Locate every Plasmodium falciparum-infected red blood cell.
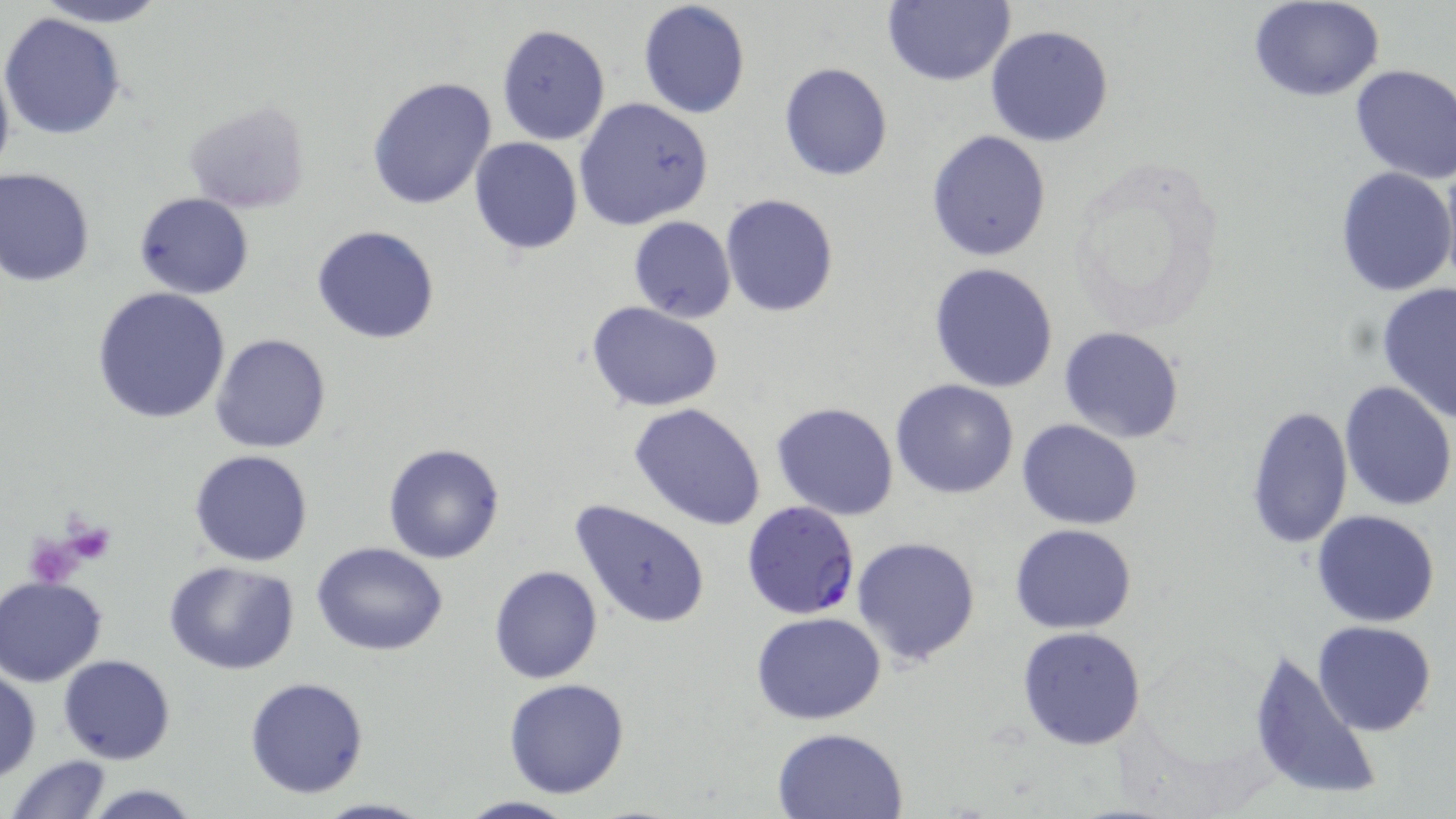

Approximate bounding boxes as named x1/y1/x2/y2 corners in pixels.
Plasmodium falciparum-infected red blood cells: (x1=740, y1=501, x2=862, y2=620).

slide_level_diagnosis: Plasmodium falciparum
stain: May-Grünwald-Giemsa
platelet_locations: 'approximate bounding boxes as named x1/y1/x2/y2 corners in pixels: (x1=61, y1=521, x2=115, y2=564), (x1=35, y1=522, x2=109, y2=579)'
magnification: 1000x
preparation: thin blood film
uninfected_red_blood_cell_locations: 'approximate bounding boxes as named x1/y1/x2/y2 corners in pixels: (x1=29, y1=0, x2=174, y2=27), (x1=636, y1=0, x2=751, y2=119), (x1=883, y1=0, x2=1016, y2=87), (x1=1249, y1=0, x2=1386, y2=102), (x1=0, y1=11, x2=128, y2=142), (x1=496, y1=23, x2=612, y2=146), (x1=985, y1=25, x2=1115, y2=148), (x1=778, y1=62, x2=893, y2=181), (x1=1350, y1=64, x2=1456, y2=184), (x1=366, y1=75, x2=498, y2=212), (x1=573, y1=97, x2=714, y2=231), (x1=183, y1=101, x2=311, y2=214), (x1=926, y1=130, x2=1051, y2=262), (x1=468, y1=137, x2=583, y2=254), (x1=1440, y1=157, x2=1456, y2=289), (x1=1335, y1=166, x2=1455, y2=297), (x1=0, y1=168, x2=96, y2=286), (x1=134, y1=193, x2=254, y2=299), (x1=721, y1=194, x2=839, y2=317), (x1=628, y1=216, x2=736, y2=323), (x1=312, y1=225, x2=441, y2=345), (x1=928, y1=261, x2=1059, y2=392), (x1=1377, y1=282, x2=1456, y2=421), (x1=91, y1=287, x2=232, y2=424), (x1=585, y1=301, x2=723, y2=413), (x1=1058, y1=326, x2=1184, y2=444), (x1=211, y1=333, x2=332, y2=454), (x1=890, y1=379, x2=1019, y2=498), (x1=1338, y1=381, x2=1455, y2=512), (x1=769, y1=401, x2=900, y2=521), (x1=627, y1=403, x2=768, y2=532), (x1=1245, y1=404, x2=1354, y2=549), (x1=1017, y1=417, x2=1143, y2=530), (x1=383, y1=443, x2=505, y2=564), (x1=190, y1=450, x2=312, y2=567), (x1=571, y1=498, x2=710, y2=628), (x1=1312, y1=509, x2=1441, y2=627), (x1=1010, y1=524, x2=1138, y2=634), (x1=852, y1=534, x2=983, y2=667), (x1=313, y1=542, x2=449, y2=656), (x1=164, y1=562, x2=299, y2=675), (x1=488, y1=565, x2=603, y2=684), (x1=1, y1=576, x2=107, y2=686), (x1=751, y1=611, x2=888, y2=725), (x1=1312, y1=619, x2=1437, y2=736), (x1=1017, y1=626, x2=1148, y2=749), (x1=1247, y1=649, x2=1383, y2=804), (x1=59, y1=654, x2=176, y2=765), (x1=0, y1=669, x2=41, y2=780), (x1=245, y1=676, x2=369, y2=798), (x1=503, y1=678, x2=630, y2=798), (x1=771, y1=727, x2=908, y2=818), (x1=7, y1=754, x2=112, y2=819), (x1=79, y1=782, x2=206, y2=818), (x1=452, y1=794, x2=581, y2=819), (x1=312, y1=797, x2=436, y2=818)'
modality: light microscopy
image_size: 1456×819 pixels
field_of_view: single